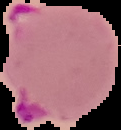 Cell region segmented out of the field of view; the surrounding area is masked to black. Image is 121×130 pixels. From a thin blood film. Malaria status: parasitized.